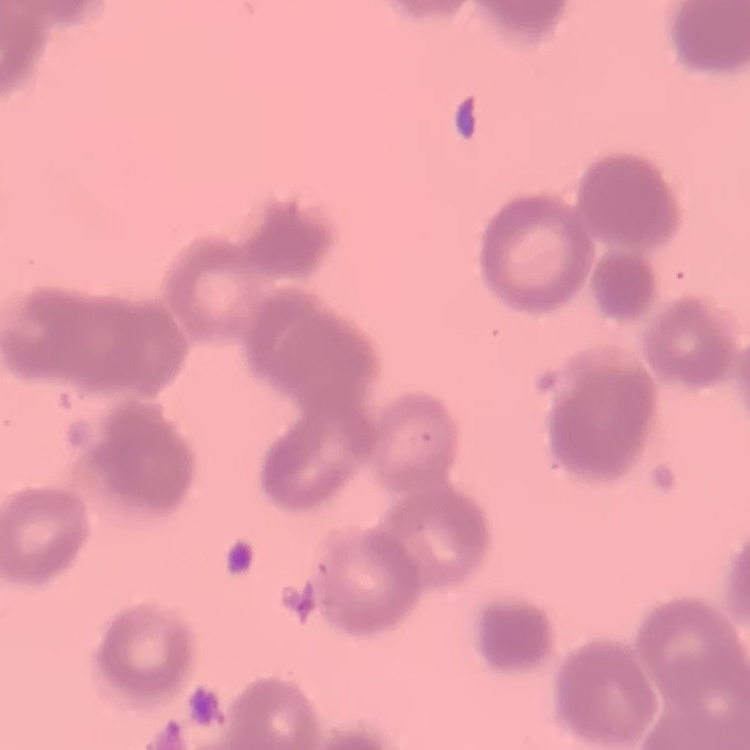
The red blood cells exhibit rouleaux formation. Thin blood smear. Field's or Giemsa stain. One tile cut from a larger photomicrograph.